Point out each Plasmodium parasite.
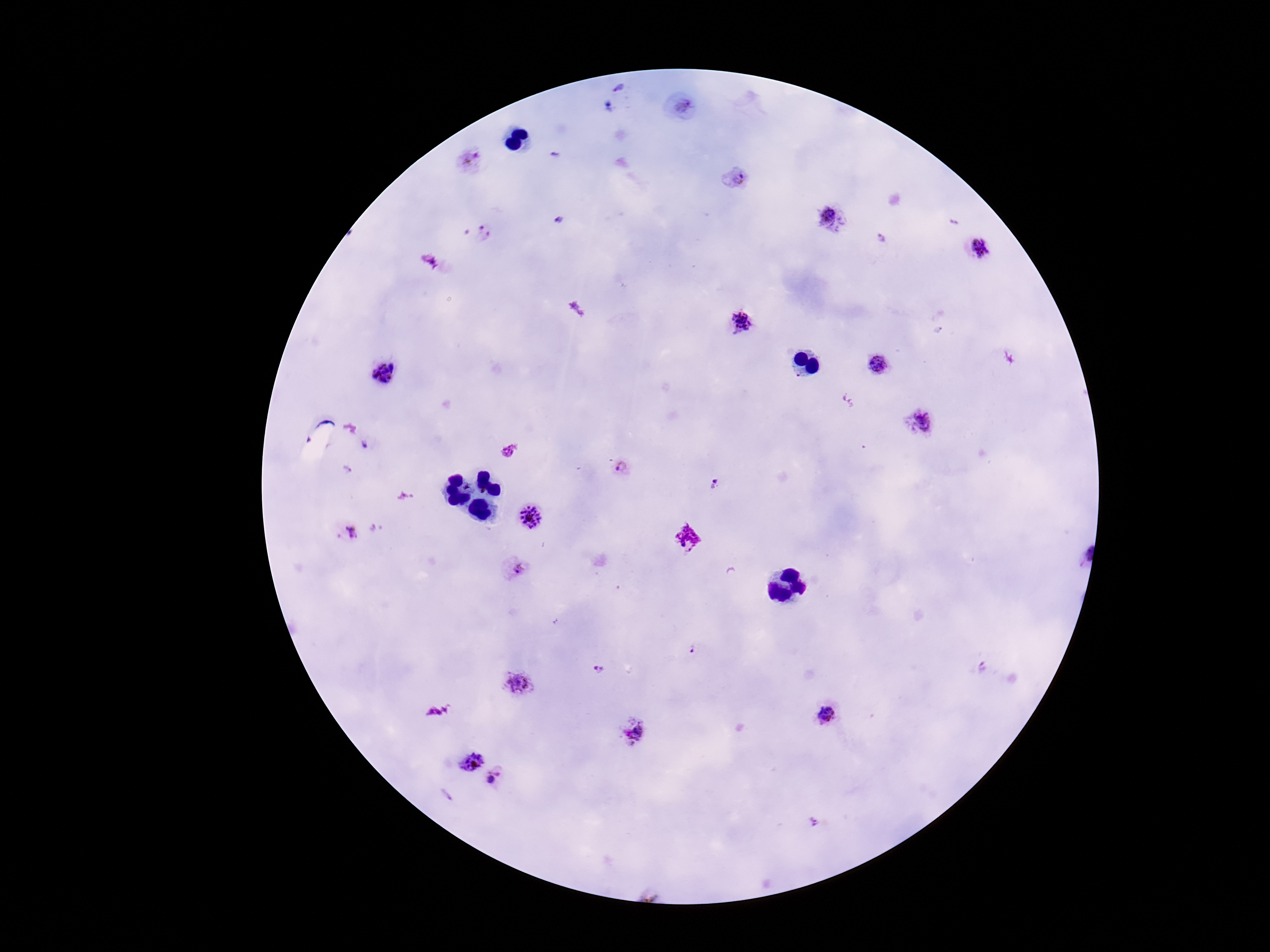

Approximate centers as {x, y} in pixels.
Plasmodium parasites: {680, 108}, {471, 163}, {735, 178}, {833, 221}, {484, 233}, {882, 240}, {977, 248}, {741, 321}, {878, 365}, {385, 372}, {922, 420}, {623, 468}, {348, 472}, {713, 485}, {530, 517}, {351, 532}, {515, 569}, {982, 668}, {599, 670}, {517, 682}, {829, 715}, {633, 733}, {470, 762}, {496, 779}, {446, 795}, {814, 821}.

patient_malaria_status: infected
preparation: thick peripheral-blood smear
stain: Giemsa
magnification: 100x
field_of_view: one from this slide
capture: smartphone camera through the microscope eyepiece
image_size: 1270×952 pixels